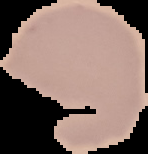
image type = segmented cell region with the area outside set to black
image size = 148×154 pixels
preparation = thin blood smear
malaria status = uninfected